Describe the morphology of the red blood cells.
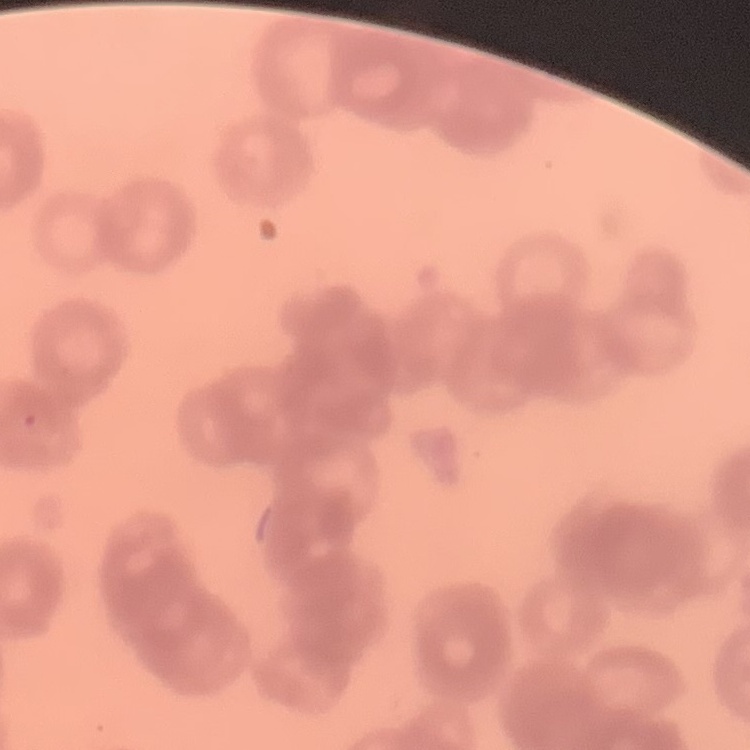
Rouleaux formation.

Summary:
  - Image type: square crop of a larger photomicrograph
  - Stain: Field's or Giemsa
  - Preparation: thin blood smear